Describe the morphology of the erythrocytes.
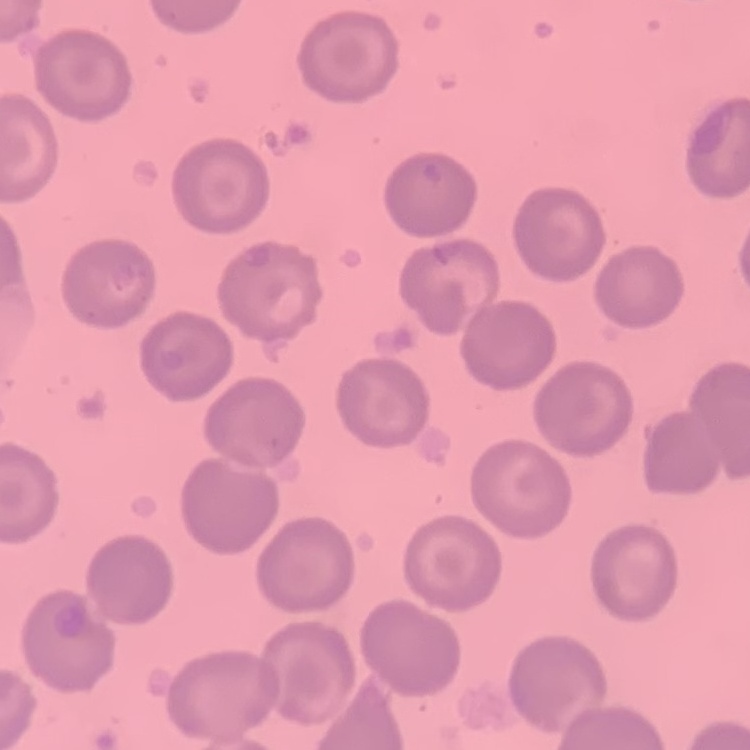

No rouleaux formation.

stain = Field's or Giemsa
image type = one tile cut from a larger photomicrograph
preparation = thin blood film